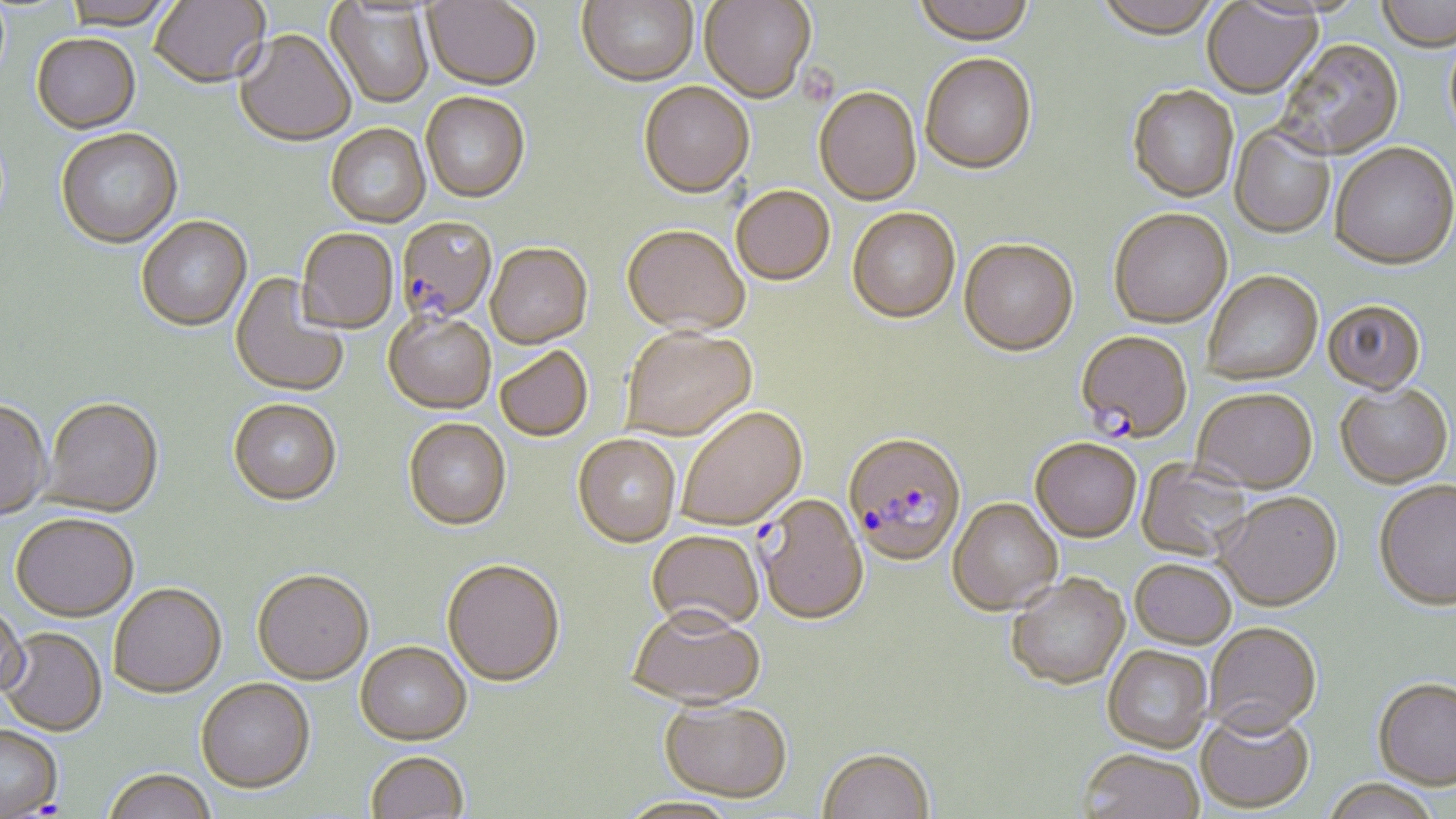 Approximate bounding boxes as (x1,y1)-(x2,y2) corner pairs in pixels. Plasmodium falciparum-infected red blood cell locations: (395,218)-(497,326), (1074,332)-(1193,444), (842,435)-(967,568). Uninfected red blood cell locations: (63,0)-(174,31), (422,0)-(541,92), (576,0)-(698,88), (699,0)-(816,105), (912,0)-(1035,49), (1094,0)-(1223,42), (1376,0)-(1455,53), (150,1)-(271,91), (325,2)-(434,108), (1201,2)-(1326,101), (234,31)-(355,149), (31,35)-(141,135), (1275,41)-(1404,161), (920,56)-(1038,177), (638,83)-(754,200), (1127,87)-(1239,203), (814,89)-(922,208), (420,94)-(530,204), (1229,125)-(1335,239), (326,126)-(430,230), (56,130)-(183,251), (1330,145)-(1456,273), (731,187)-(835,287), (847,209)-(960,326), (1108,210)-(1233,330), (136,218)-(252,333), (622,228)-(749,339), (296,229)-(398,335), (959,240)-(1079,359), (485,244)-(593,352), (1203,272)-(1323,386), (229,273)-(349,399), (1322,302)-(1426,396), (384,315)-(496,416), (621,328)-(757,443), (495,347)-(593,443), (1335,385)-(1452,489), (1192,390)-(1318,495), (43,400)-(163,519), (228,401)-(341,508), (0,402)-(51,523), (677,408)-(807,532), (403,420)-(511,532), (572,436)-(680,549), (1030,439)-(1142,544), (1136,458)-(1252,562), (1373,482)-(1456,612), (1214,494)-(1342,613), (757,495)-(868,627), (948,499)-(1063,617), (10,516)-(138,624), (647,530)-(764,635), (1130,561)-(1236,650), (442,562)-(565,690), (252,573)-(373,688), (1006,575)-(1131,692), (109,585)-(226,701), (0,604)-(29,702), (628,609)-(765,712), (1205,623)-(1321,739), (0,629)-(107,738), (355,645)-(471,747), (1102,646)-(1213,755), (196,680)-(316,797), (1372,680)-(1456,792), (659,702)-(792,806), (1196,709)-(1314,814), (0,727)-(62,817), (817,750)-(935,819), (1077,751)-(1204,819), (366,754)-(469,819), (103,772)-(217,819), (1321,780)-(1442,819). Slide-level diagnosis: Plasmodium falciparum. One field of a larger specimen. Optical microscopy. 1000x magnification. Image is 1456×819 pixels. Thin blood film. May-Grünwald-Giemsa-stained preparation.